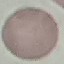 Malaria status: uninfected. Cell patch, automatically extracted from a larger field of view and resized to 64 × 64 pixels. Acquired by smartphone through the microscope eyepiece. Thin blood film. Giemsa-stained preparation.